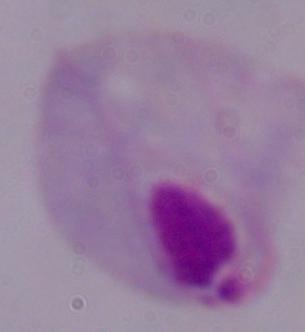
Summary:
  - Modality: micrograph
  - Identification: trichomonad
  - Magnification: 1000x